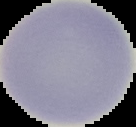

From a thin blood smear. Malaria status: uninfected. Image is 136×127 pixels. Segmented cell region on a black background.